Identify the cell.
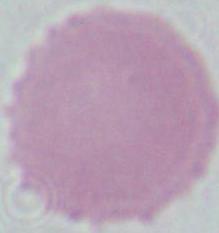
An erythrocyte.

1000x magnification. Micrograph.